Assess this cell for malaria.
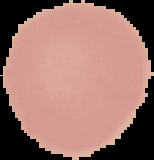
It is uninfected.

From a thin blood film. Image is 154×160 pixels. Segmented cell region on a black background.